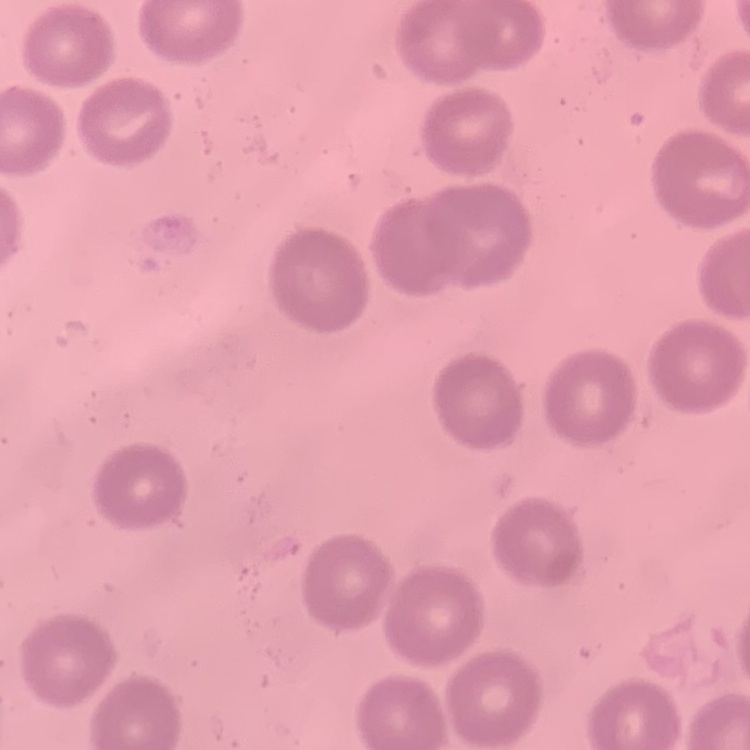

The red blood cells exhibit no rouleaux formation. Stained with either Field's or Giemsa. Thin blood film. One tile cut from a larger photomicrograph.